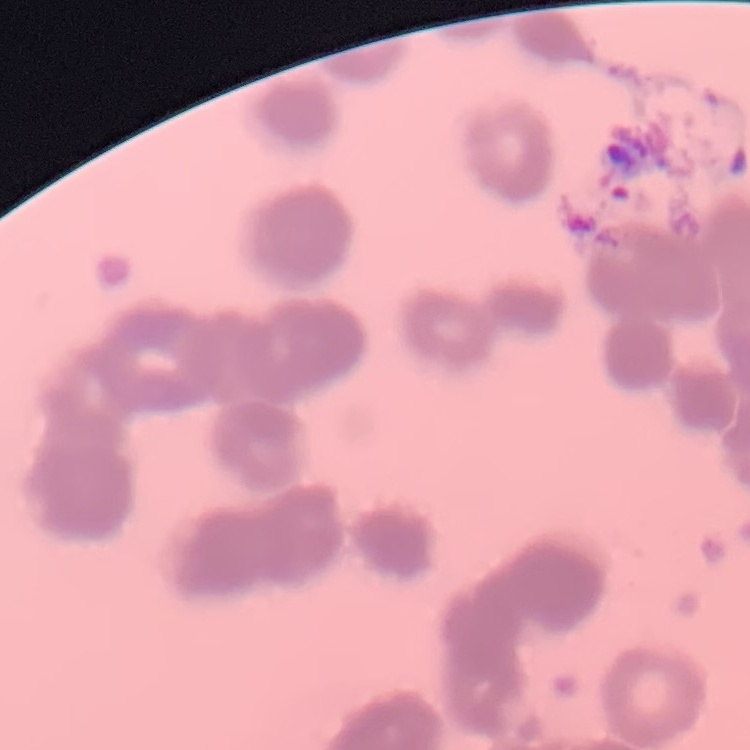 The red blood cells show rouleaux formation. Thin blood smear. One tile cut from a larger photomicrograph. Field's or Giemsa stain.